Give the extent of all Plasmodium falciparum-infected red blood cells.
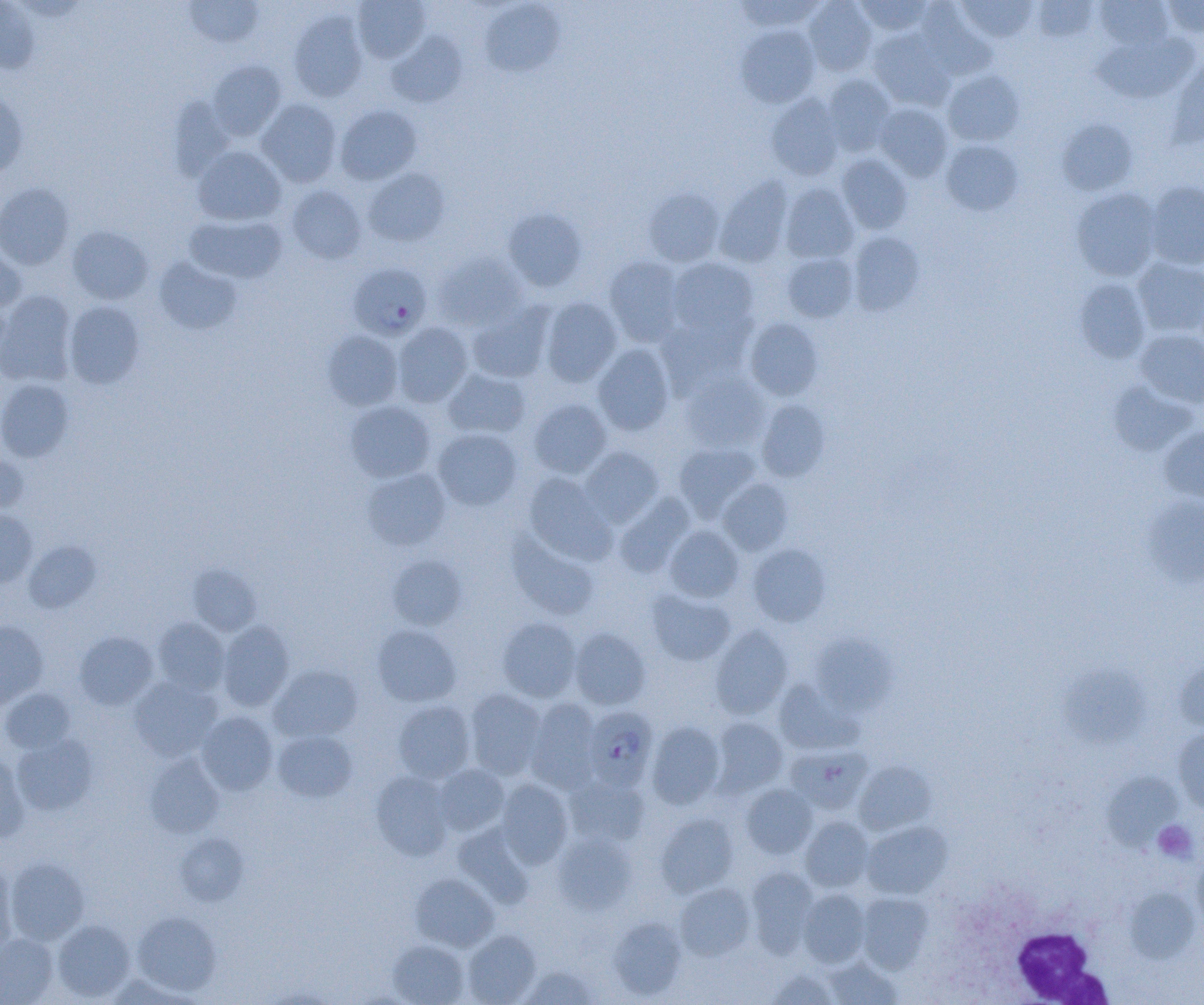
Approximate bounding boxes as named x1/y1/x2/y2 corners in pixels.
Plasmodium falciparum-infected red blood cells: (x1=348, y1=261, x2=431, y2=339), (x1=589, y1=706, x2=665, y2=791).

slide-level diagnosis = Plasmodium falciparum
white blood cell locations = approximate bounding boxes as named x1/y1/x2/y2 corners in pixels: (x1=1010, y1=924, x2=1114, y2=1003)
field of view = one of a larger specimen
uninfected red blood cell locations = approximate bounding boxes as named x1/y1/x2/y2 corners in pixels: (x1=183, y1=0, x2=264, y2=48), (x1=733, y1=0, x2=825, y2=31), (x1=804, y1=0, x2=877, y2=76), (x1=854, y1=0, x2=934, y2=36), (x1=958, y1=0, x2=1037, y2=43), (x1=1031, y1=0, x2=1098, y2=42), (x1=1095, y1=0, x2=1173, y2=50), (x1=0, y1=1, x2=39, y2=74), (x1=353, y1=1, x2=430, y2=62), (x1=479, y1=1, x2=564, y2=77), (x1=1163, y1=1, x2=1204, y2=38), (x1=916, y1=2, x2=995, y2=80), (x1=289, y1=11, x2=368, y2=102), (x1=737, y1=26, x2=819, y2=108), (x1=867, y1=29, x2=954, y2=111), (x1=386, y1=31, x2=468, y2=107), (x1=1094, y1=32, x2=1199, y2=103), (x1=1170, y1=55, x2=1204, y2=146), (x1=208, y1=60, x2=286, y2=140), (x1=942, y1=70, x2=1024, y2=146), (x1=822, y1=75, x2=896, y2=156), (x1=0, y1=91, x2=28, y2=178), (x1=766, y1=93, x2=846, y2=180), (x1=169, y1=95, x2=235, y2=181), (x1=256, y1=99, x2=342, y2=187), (x1=875, y1=103, x2=953, y2=181), (x1=335, y1=105, x2=422, y2=185), (x1=1056, y1=119, x2=1137, y2=196), (x1=941, y1=140, x2=1023, y2=215), (x1=192, y1=146, x2=287, y2=226), (x1=836, y1=154, x2=913, y2=234), (x1=363, y1=167, x2=450, y2=247), (x1=716, y1=176, x2=793, y2=268), (x1=1145, y1=180, x2=1204, y2=270), (x1=0, y1=183, x2=75, y2=270), (x1=780, y1=184, x2=859, y2=263), (x1=286, y1=185, x2=367, y2=264), (x1=643, y1=188, x2=724, y2=267), (x1=1071, y1=188, x2=1162, y2=281), (x1=503, y1=207, x2=587, y2=292), (x1=184, y1=213, x2=287, y2=284), (x1=67, y1=226, x2=153, y2=304), (x1=847, y1=231, x2=924, y2=315), (x1=0, y1=243, x2=28, y2=314), (x1=433, y1=253, x2=528, y2=332), (x1=783, y1=253, x2=858, y2=322), (x1=604, y1=256, x2=685, y2=346), (x1=153, y1=257, x2=242, y2=335), (x1=667, y1=257, x2=758, y2=338), (x1=1133, y1=259, x2=1204, y2=337), (x1=1074, y1=277, x2=1151, y2=364), (x1=0, y1=291, x2=76, y2=387), (x1=539, y1=297, x2=622, y2=387), (x1=64, y1=301, x2=145, y2=388), (x1=467, y1=303, x2=553, y2=383), (x1=455, y1=305, x2=539, y2=439), (x1=657, y1=313, x2=752, y2=397), (x1=744, y1=318, x2=823, y2=400), (x1=393, y1=322, x2=473, y2=407), (x1=1134, y1=328, x2=1204, y2=408), (x1=322, y1=330, x2=404, y2=411), (x1=593, y1=344, x2=675, y2=435), (x1=443, y1=368, x2=531, y2=440), (x1=682, y1=373, x2=770, y2=452), (x1=0, y1=378, x2=74, y2=462), (x1=1107, y1=380, x2=1198, y2=456), (x1=528, y1=398, x2=612, y2=478), (x1=756, y1=400, x2=830, y2=481), (x1=345, y1=401, x2=435, y2=482), (x1=1158, y1=425, x2=1204, y2=503), (x1=432, y1=428, x2=522, y2=511), (x1=673, y1=443, x2=760, y2=520), (x1=580, y1=446, x2=664, y2=527), (x1=0, y1=454, x2=29, y2=513), (x1=362, y1=468, x2=451, y2=550), (x1=522, y1=472, x2=616, y2=565), (x1=717, y1=478, x2=793, y2=555), (x1=613, y1=493, x2=696, y2=578), (x1=1142, y1=495, x2=1204, y2=587), (x1=0, y1=510, x2=37, y2=587), (x1=664, y1=525, x2=744, y2=602), (x1=507, y1=529, x2=600, y2=621), (x1=24, y1=540, x2=100, y2=613), (x1=747, y1=543, x2=831, y2=627), (x1=387, y1=555, x2=467, y2=630), (x1=188, y1=564, x2=261, y2=636), (x1=647, y1=589, x2=735, y2=666), (x1=497, y1=617, x2=581, y2=702), (x1=152, y1=618, x2=230, y2=695), (x1=0, y1=620, x2=48, y2=706), (x1=217, y1=621, x2=294, y2=711), (x1=372, y1=624, x2=461, y2=707), (x1=710, y1=624, x2=794, y2=719), (x1=569, y1=627, x2=651, y2=710), (x1=74, y1=631, x2=157, y2=709), (x1=809, y1=632, x2=897, y2=716), (x1=1175, y1=657, x2=1204, y2=732), (x1=1060, y1=663, x2=1149, y2=748), (x1=269, y1=665, x2=363, y2=742), (x1=129, y1=676, x2=222, y2=761), (x1=773, y1=679, x2=862, y2=755), (x1=1, y1=687, x2=76, y2=753), (x1=465, y1=689, x2=547, y2=779), (x1=525, y1=698, x2=601, y2=793), (x1=393, y1=700, x2=476, y2=782), (x1=196, y1=711, x2=277, y2=795), (x1=710, y1=717, x2=788, y2=797), (x1=646, y1=721, x2=725, y2=809), (x1=1172, y1=728, x2=1204, y2=813), (x1=272, y1=729, x2=357, y2=802), (x1=11, y1=735, x2=97, y2=816), (x1=786, y1=744, x2=872, y2=814), (x1=0, y1=753, x2=30, y2=843), (x1=145, y1=753, x2=224, y2=837), (x1=854, y1=760, x2=936, y2=836), (x1=434, y1=764, x2=509, y2=835), (x1=370, y1=770, x2=454, y2=861), (x1=1102, y1=772, x2=1183, y2=852), (x1=564, y1=775, x2=650, y2=848), (x1=495, y1=779, x2=573, y2=868), (x1=741, y1=783, x2=818, y2=859), (x1=655, y1=813, x2=739, y2=897), (x1=799, y1=816, x2=874, y2=892), (x1=863, y1=821, x2=952, y2=899), (x1=453, y1=823, x2=534, y2=909), (x1=175, y1=833, x2=248, y2=905), (x1=552, y1=834, x2=636, y2=915), (x1=1192, y1=853, x2=1204, y2=935), (x1=5, y1=857, x2=90, y2=945), (x1=0, y1=860, x2=17, y2=953), (x1=745, y1=866, x2=819, y2=957), (x1=410, y1=874, x2=499, y2=952), (x1=675, y1=882, x2=755, y2=960), (x1=798, y1=888, x2=870, y2=967), (x1=1124, y1=888, x2=1199, y2=963), (x1=856, y1=892, x2=933, y2=974), (x1=132, y1=911, x2=221, y2=996), (x1=608, y1=917, x2=686, y2=999), (x1=52, y1=919, x2=135, y2=1001), (x1=462, y1=930, x2=540, y2=1004), (x1=0, y1=934, x2=59, y2=1004), (x1=388, y1=939, x2=469, y2=1004), (x1=823, y1=956, x2=902, y2=1004), (x1=522, y1=965, x2=599, y2=1004), (x1=766, y1=968, x2=839, y2=1004)
platelet locations = approximate bounding boxes as named x1/y1/x2/y2 corners in pixels: (x1=1153, y1=820, x2=1198, y2=862)
modality = light microscopy
magnification = 1000x
preparation = thin blood film
image size = 1204×1005 pixels